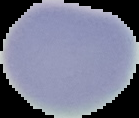
image size = 139×118 pixels
image type = segmented cell region on a black background
preparation = thin blood film
malaria status = uninfected